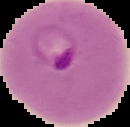
From a thin blood smear. Image is 130×127 pixels. The area outside the segmented cell region is set to black. Result: Plasmodium parasites detected.